Draw a bounding box around every artifact (platelet-like body, stain precipitate, or debris).
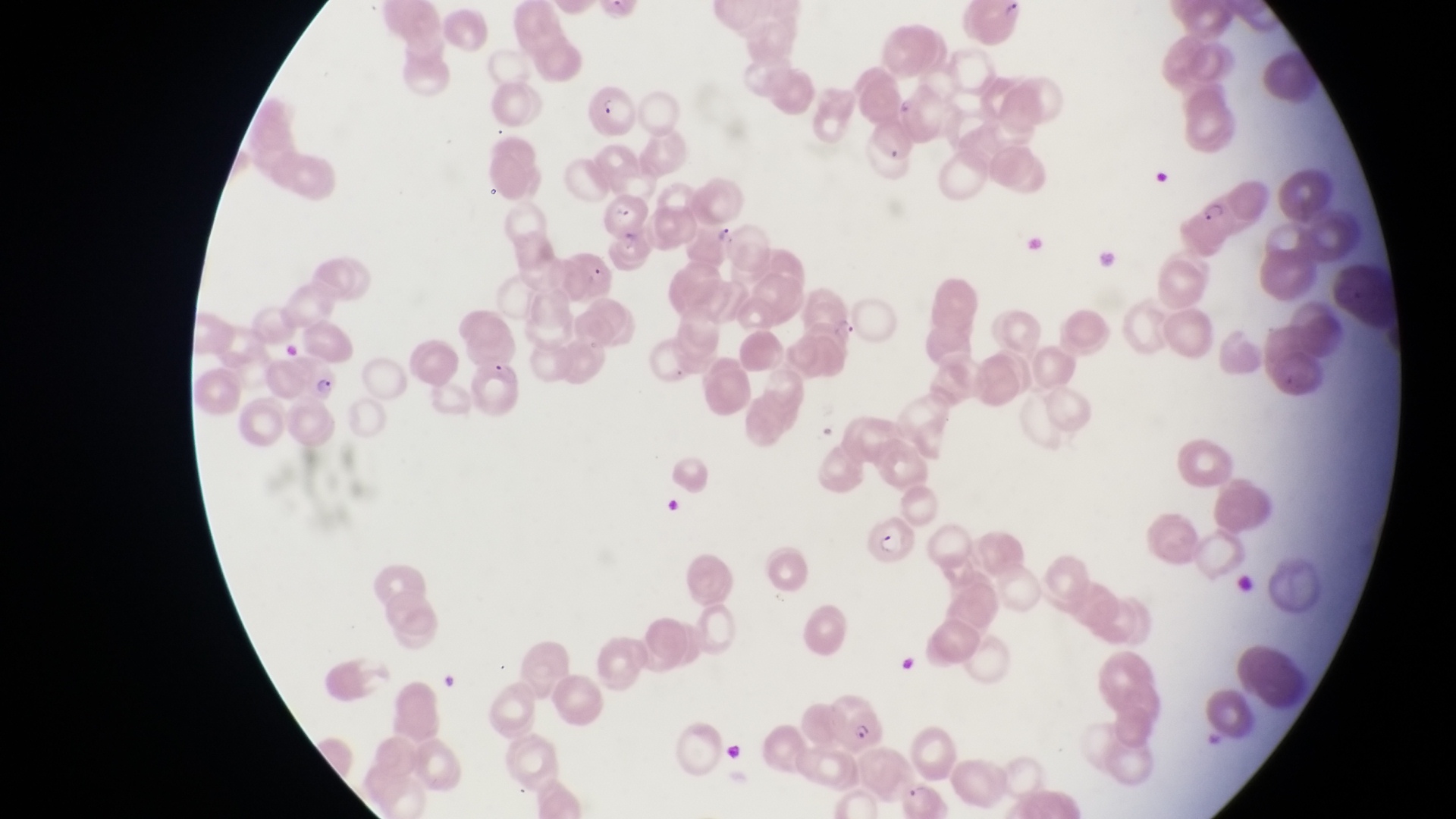
Approximate bounding boxes as [left, top, right, bottom] in pixels.
Artifacts (platelet-like body, stain precipitate, or debris): [667, 495, 699, 527].

image size = 1456×819 pixels
country = Uganda
magnification = 1000x
parasitised red blood cell locations = approximate bounding boxes as [left, top, right, bottom] in pixels: [584, 71, 639, 138], [1197, 184, 1247, 243], [604, 188, 647, 240], [690, 209, 743, 268], [281, 350, 352, 405], [871, 513, 923, 565], [824, 689, 896, 753]
capture = smartphone photograph through the eyepiece of an Olympus CX-23 microscope
preparation = thin blood film
field of view = single